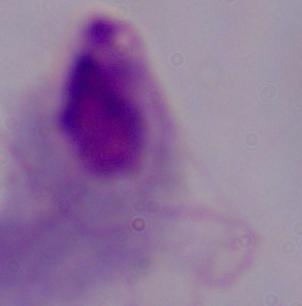

Photomicrograph. 1000x magnification. A trichomonad is seen.